Assess this cell for malaria.
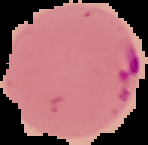

It is parasitized.

Summary:
  - Image type: segmented cell region with the area outside set to black
  - Image size: 148×145 pixels
  - Preparation: thin blood film